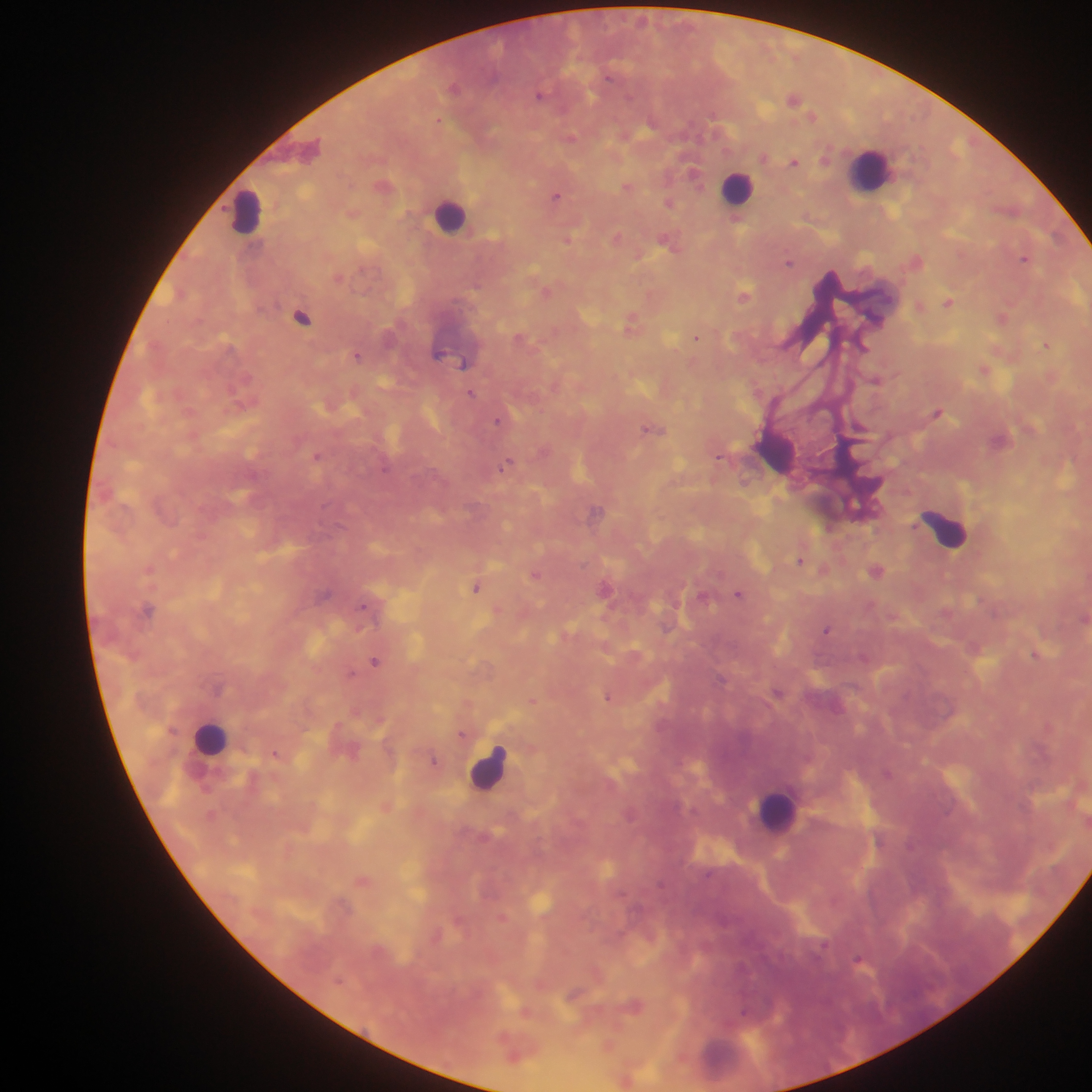
leukocyte locations = approximate centers as {x, y} in pixels: {871, 170}, {737, 188}, {246, 212}, {449, 215}, {775, 451}, {946, 529}, {210, 738}, {488, 769}, {775, 811}
capture = mobile-phone photograph through a microscope
image size = 1092×1092 pixels
country = Ghana
preparation = thick blood film
field of view = single
malaria parasite locations = approximate centers as {x, y} in pixels: {455, 87}, {541, 95}, {793, 98}, {570, 137}, {764, 157}, {794, 160}, {694, 172}, {384, 185}, {628, 186}, {556, 195}, {669, 202}, {737, 218}, {617, 237}, {568, 239}, {670, 242}, {1025, 259}, {917, 260}, {788, 262}, {339, 277}, {547, 291}, {181, 293}, {744, 294}, {949, 301}, {919, 306}, {1002, 316}, {303, 317}, {633, 322}, {697, 336}, {523, 338}, {1047, 344}, {439, 352}, {358, 355}, {464, 364}, {985, 369}, {876, 379}, {472, 394}, {938, 411}, {500, 420}, {653, 429}, {317, 455}, {719, 456}, {508, 464}, {597, 512}, {801, 560}, {824, 568}, {877, 570}, {536, 574}, {476, 586}, {606, 588}, {739, 593}, {326, 595}, {704, 596}, {148, 610}, {498, 610}, {1084, 617}, {827, 629}, {1036, 655}, {375, 661}, {779, 692}, {609, 696}, {533, 700}, {468, 702}, {462, 734}, {276, 752}, {435, 760}, {386, 806}, {363, 881}, {859, 960}, {576, 993}, {635, 1005}, {526, 1010}, {608, 1045}, {514, 1053}, {627, 1079}